Locate every malaria parasite by life-cycle stage, and every leukocyte.
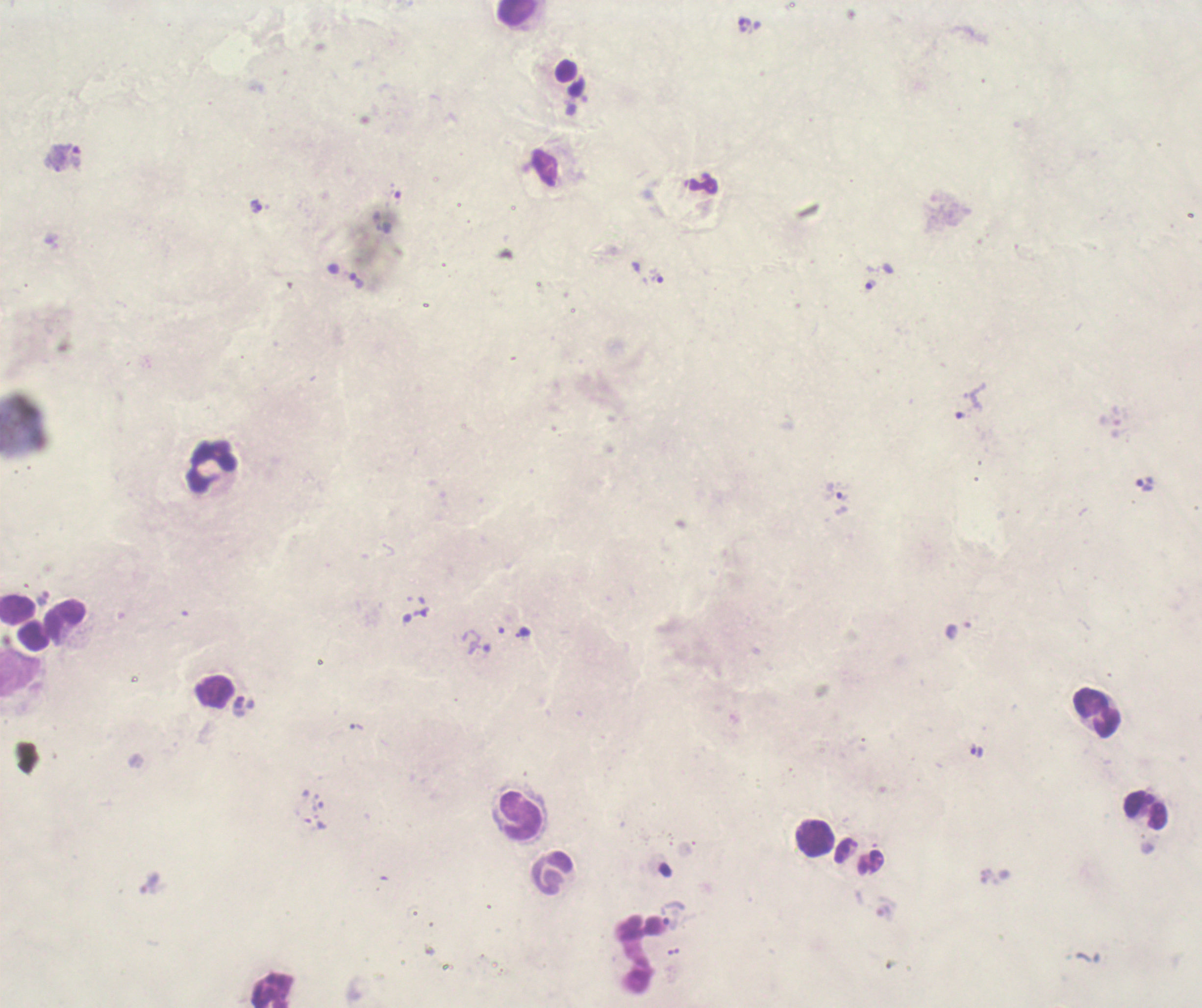
Approximate object centers, in pixels from the top-left corner.
Trophozoites: (x=745, y=26), (x=256, y=207), (x=657, y=278), (x=357, y=282), (x=871, y=285), (x=971, y=401), (x=1146, y=486), (x=842, y=498), (x=977, y=752).
No schizont or gametocyte forms observed.
Leukocytes: (x=519, y=13), (x=212, y=467), (x=1098, y=713), (x=1146, y=809), (x=521, y=817), (x=816, y=838), (x=550, y=872).

Previously used in an actual diagnosis. Thick blood smear. Coloration quality: bad. Romanowsky-stained preparation. Single field of view. Background quality: unsatisfactory. 100x magnification. Image is 1202×1008 pixels.